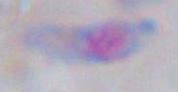
Summary:
  - Modality: photomicrograph
  - Identification: Toxoplasma gondii
  - Magnification: 1000x